Identify the cell.
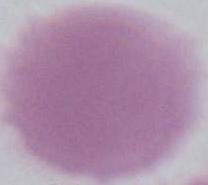

An erythrocyte.

Summary:
  - Modality: photomicrograph
  - Magnification: 1000x